Assess this cell for malaria.
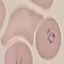

Parasitized.

capture = smartphone camera at the microscope eyepiece
preparation = thin smear
stain = Giemsa
image type = cell patch, automatically extracted from a larger field of view and resized to 64 × 64 pixels